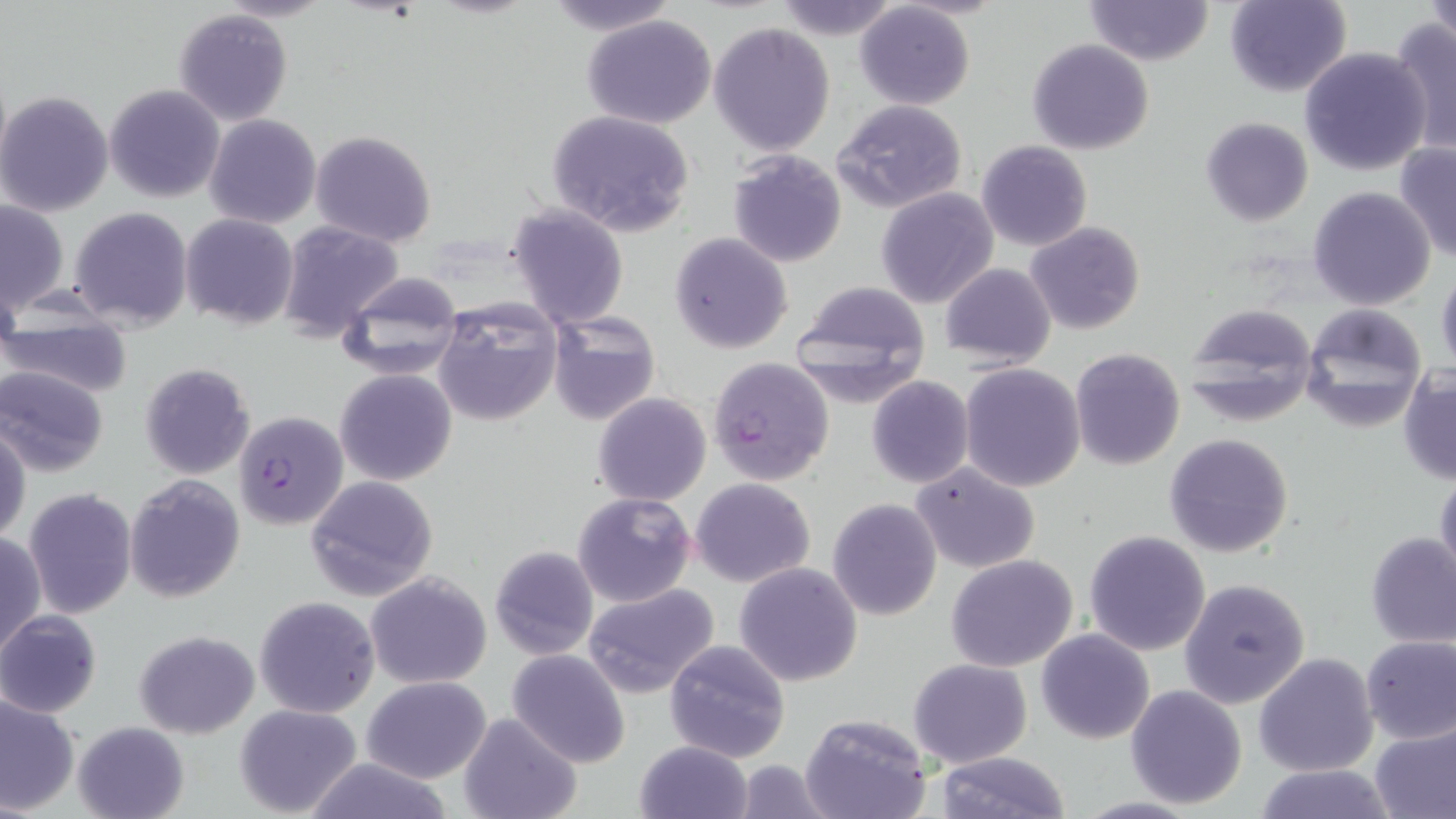

Approximate bounding boxes as named x1/y1/x2/y2 corners in pixels. Uninfected red blood cell locations: (x1=545, y1=0, x2=677, y2=34), (x1=771, y1=0, x2=902, y2=40), (x1=1084, y1=0, x2=1213, y2=66), (x1=1225, y1=0, x2=1350, y2=98), (x1=1425, y1=0, x2=1454, y2=47), (x1=854, y1=2, x2=976, y2=111), (x1=172, y1=8, x2=293, y2=125), (x1=581, y1=14, x2=718, y2=129), (x1=1387, y1=18, x2=1455, y2=156), (x1=708, y1=21, x2=835, y2=156), (x1=1027, y1=39, x2=1155, y2=155), (x1=1301, y1=45, x2=1433, y2=176), (x1=104, y1=83, x2=226, y2=203), (x1=1, y1=91, x2=113, y2=216), (x1=832, y1=100, x2=969, y2=215), (x1=545, y1=109, x2=696, y2=236), (x1=205, y1=113, x2=321, y2=228), (x1=1200, y1=116, x2=1314, y2=227), (x1=310, y1=129, x2=437, y2=245), (x1=976, y1=140, x2=1092, y2=251), (x1=1395, y1=142, x2=1456, y2=263), (x1=726, y1=150, x2=848, y2=268), (x1=1307, y1=186, x2=1436, y2=311), (x1=876, y1=188, x2=1000, y2=310), (x1=0, y1=197, x2=68, y2=316), (x1=506, y1=202, x2=629, y2=328), (x1=69, y1=206, x2=193, y2=332), (x1=181, y1=213, x2=298, y2=329), (x1=277, y1=221, x2=403, y2=342), (x1=1026, y1=221, x2=1145, y2=334), (x1=670, y1=232, x2=794, y2=355), (x1=938, y1=262, x2=1055, y2=367), (x1=1435, y1=266, x2=1456, y2=377), (x1=336, y1=270, x2=465, y2=382), (x1=790, y1=279, x2=932, y2=404), (x1=431, y1=298, x2=563, y2=427), (x1=1186, y1=304, x2=1320, y2=425), (x1=1301, y1=305, x2=1428, y2=431), (x1=547, y1=309, x2=662, y2=428), (x1=1, y1=318, x2=135, y2=400), (x1=1071, y1=348, x2=1185, y2=469), (x1=139, y1=362, x2=255, y2=480), (x1=959, y1=363, x2=1086, y2=492), (x1=0, y1=365, x2=111, y2=478), (x1=1398, y1=367, x2=1456, y2=486), (x1=335, y1=368, x2=457, y2=485), (x1=867, y1=376, x2=974, y2=488), (x1=592, y1=392, x2=712, y2=506), (x1=0, y1=421, x2=29, y2=545), (x1=1164, y1=433, x2=1294, y2=558), (x1=910, y1=463, x2=1041, y2=572), (x1=1434, y1=469, x2=1456, y2=585), (x1=125, y1=473, x2=245, y2=603), (x1=305, y1=475, x2=439, y2=603), (x1=691, y1=477, x2=815, y2=587), (x1=23, y1=488, x2=138, y2=618), (x1=573, y1=492, x2=695, y2=607), (x1=828, y1=498, x2=941, y2=620), (x1=1084, y1=530, x2=1211, y2=655), (x1=0, y1=532, x2=46, y2=662), (x1=1365, y1=532, x2=1455, y2=649), (x1=488, y1=545, x2=599, y2=661), (x1=495, y1=546, x2=610, y2=771), (x1=947, y1=555, x2=1080, y2=672), (x1=733, y1=562, x2=863, y2=686), (x1=365, y1=572, x2=493, y2=691), (x1=1178, y1=577, x2=1312, y2=709), (x1=582, y1=583, x2=721, y2=701), (x1=254, y1=596, x2=380, y2=717), (x1=0, y1=611, x2=102, y2=718), (x1=1037, y1=629, x2=1155, y2=745), (x1=134, y1=630, x2=260, y2=737), (x1=1360, y1=634, x2=1455, y2=743), (x1=663, y1=640, x2=792, y2=763), (x1=507, y1=649, x2=630, y2=767), (x1=1254, y1=652, x2=1379, y2=775), (x1=909, y1=659, x2=1032, y2=768), (x1=363, y1=676, x2=491, y2=783), (x1=1125, y1=684, x2=1249, y2=809), (x1=0, y1=695, x2=80, y2=816), (x1=234, y1=703, x2=363, y2=818), (x1=459, y1=711, x2=583, y2=819), (x1=799, y1=713, x2=931, y2=819), (x1=73, y1=719, x2=189, y2=819), (x1=1369, y1=723, x2=1456, y2=819), (x1=634, y1=740, x2=754, y2=819), (x1=934, y1=751, x2=1071, y2=819), (x1=304, y1=755, x2=453, y2=819), (x1=732, y1=760, x2=833, y2=819), (x1=1252, y1=763, x2=1399, y2=819), (x1=1069, y1=795, x2=1207, y2=818). Plasmodium falciparum-infected red blood cell locations: (x1=707, y1=357, x2=836, y2=485), (x1=232, y1=410, x2=348, y2=531). Slide-level diagnosis: Plasmodium falciparum. May-Grünwald-Giemsa stain. Captured at 1000x magnification. Light microscopy. One field of a larger specimen. Image is 1456×819 pixels. Thin blood smear.